Assess this cell for malaria.
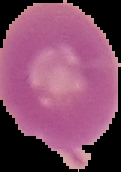
It is uninfected.

Summary:
  - Image size: 121×172 pixels
  - Preparation: thin blood film
  - Image type: segmented cell region with the area outside set to black